Outline each blood parasite and name the species.
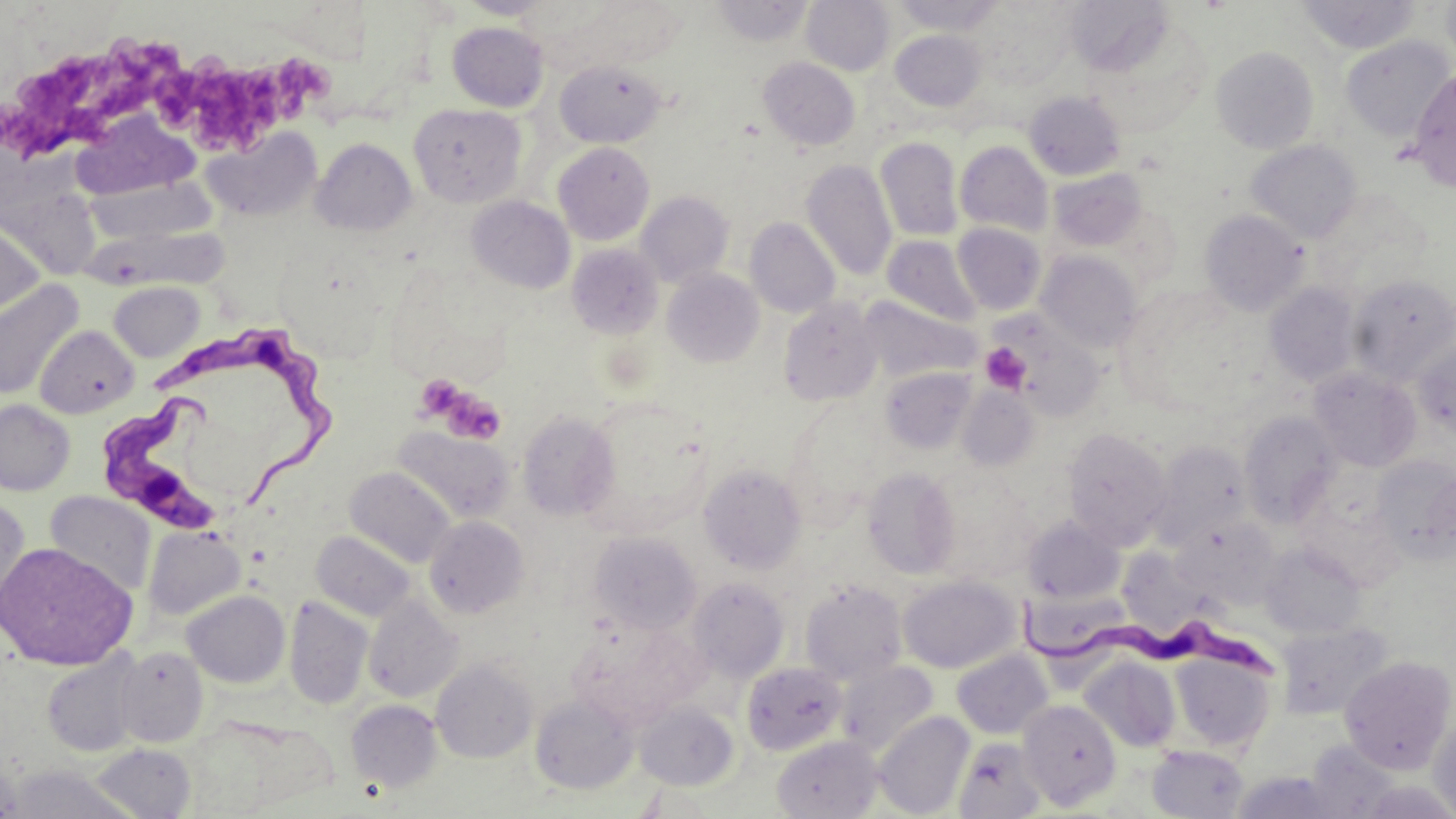

Approximate bounding boxes as named x1/y1/x2/y2 corners in pixels.
Trypanosoma brucei: (x1=154, y1=325, x2=332, y2=505), (x1=100, y1=397, x2=228, y2=534), (x1=1016, y1=596, x2=1282, y2=688).
No Plasmodium falciparum, Plasmodium ovale, Plasmodium malariae, Plasmodium vivax, or Babesia divergens observed.

Platelet locations: (x1=0, y1=34, x2=173, y2=157), (x1=154, y1=50, x2=331, y2=144), (x1=979, y1=343, x2=1031, y2=394), (x1=414, y1=374, x2=463, y2=420), (x1=438, y1=387, x2=506, y2=445). Uninfected red blood cell locations: (x1=459, y1=0, x2=552, y2=19), (x1=711, y1=0, x2=815, y2=47), (x1=801, y1=0, x2=894, y2=75), (x1=890, y1=0, x2=1006, y2=35), (x1=1296, y1=0, x2=1421, y2=54), (x1=1441, y1=0, x2=1456, y2=74), (x1=575, y1=2, x2=686, y2=67), (x1=968, y1=2, x2=1080, y2=90), (x1=1065, y1=2, x2=1195, y2=99), (x1=447, y1=22, x2=548, y2=112), (x1=890, y1=30, x2=986, y2=111), (x1=1339, y1=35, x2=1455, y2=143), (x1=1211, y1=45, x2=1319, y2=154), (x1=758, y1=57, x2=861, y2=151), (x1=555, y1=60, x2=667, y2=148), (x1=1407, y1=67, x2=1456, y2=192), (x1=1023, y1=90, x2=1126, y2=181), (x1=409, y1=104, x2=525, y2=207), (x1=70, y1=112, x2=198, y2=201), (x1=203, y1=127, x2=322, y2=221), (x1=875, y1=136, x2=964, y2=241), (x1=311, y1=138, x2=417, y2=235), (x1=1246, y1=139, x2=1363, y2=243), (x1=955, y1=141, x2=1053, y2=237), (x1=553, y1=142, x2=655, y2=245), (x1=801, y1=159, x2=896, y2=282), (x1=1049, y1=168, x2=1148, y2=251), (x1=85, y1=177, x2=215, y2=243), (x1=0, y1=181, x2=119, y2=274), (x1=635, y1=190, x2=734, y2=287), (x1=466, y1=195, x2=576, y2=294), (x1=1199, y1=209, x2=1309, y2=316), (x1=0, y1=215, x2=45, y2=319), (x1=745, y1=217, x2=840, y2=318), (x1=952, y1=222, x2=1047, y2=315), (x1=87, y1=228, x2=239, y2=289), (x1=882, y1=235, x2=982, y2=326), (x1=567, y1=244, x2=663, y2=339), (x1=1036, y1=251, x2=1144, y2=353), (x1=662, y1=269, x2=764, y2=368), (x1=1348, y1=273, x2=1455, y2=383), (x1=0, y1=279, x2=84, y2=401), (x1=109, y1=281, x2=204, y2=362), (x1=1265, y1=282, x2=1361, y2=387), (x1=858, y1=297, x2=980, y2=383), (x1=778, y1=299, x2=883, y2=406), (x1=992, y1=312, x2=1107, y2=422), (x1=36, y1=325, x2=139, y2=418), (x1=1412, y1=335, x2=1456, y2=440), (x1=879, y1=366, x2=976, y2=454), (x1=1308, y1=366, x2=1421, y2=472), (x1=957, y1=384, x2=1039, y2=471), (x1=576, y1=398, x2=713, y2=538), (x1=0, y1=399, x2=75, y2=495), (x1=781, y1=401, x2=886, y2=521), (x1=517, y1=411, x2=620, y2=521), (x1=1239, y1=411, x2=1342, y2=526), (x1=393, y1=426, x2=515, y2=524), (x1=1062, y1=426, x2=1172, y2=548), (x1=1151, y1=441, x2=1253, y2=548), (x1=1372, y1=456, x2=1456, y2=560), (x1=699, y1=463, x2=806, y2=574), (x1=345, y1=466, x2=457, y2=568), (x1=862, y1=466, x2=961, y2=579), (x1=922, y1=469, x2=1037, y2=581), (x1=45, y1=492, x2=156, y2=598), (x1=0, y1=495, x2=30, y2=618), (x1=1021, y1=515, x2=1125, y2=605), (x1=424, y1=516, x2=530, y2=618), (x1=1173, y1=517, x2=1281, y2=604), (x1=143, y1=527, x2=245, y2=620), (x1=311, y1=531, x2=416, y2=622), (x1=589, y1=531, x2=702, y2=634), (x1=1114, y1=541, x2=1216, y2=637), (x1=0, y1=542, x2=137, y2=670), (x1=1260, y1=542, x2=1366, y2=639), (x1=898, y1=574, x2=1020, y2=673), (x1=687, y1=577, x2=789, y2=682), (x1=800, y1=580, x2=907, y2=684), (x1=182, y1=590, x2=290, y2=688), (x1=363, y1=595, x2=463, y2=703), (x1=1027, y1=596, x2=1130, y2=690), (x1=283, y1=597, x2=373, y2=710), (x1=570, y1=620, x2=705, y2=729), (x1=1275, y1=621, x2=1392, y2=720), (x1=115, y1=646, x2=208, y2=747), (x1=952, y1=649, x2=1053, y2=739), (x1=41, y1=650, x2=144, y2=757), (x1=1170, y1=652, x2=1276, y2=752), (x1=1339, y1=655, x2=1455, y2=773), (x1=1080, y1=656, x2=1181, y2=752), (x1=431, y1=659, x2=537, y2=763), (x1=837, y1=660, x2=938, y2=756), (x1=741, y1=662, x2=847, y2=755), (x1=530, y1=693, x2=640, y2=794), (x1=1019, y1=699, x2=1122, y2=809), (x1=346, y1=700, x2=443, y2=793), (x1=634, y1=701, x2=739, y2=790), (x1=1428, y1=710, x2=1456, y2=816), (x1=873, y1=711, x2=974, y2=818), (x1=772, y1=735, x2=883, y2=818), (x1=953, y1=736, x2=1047, y2=819), (x1=1303, y1=740, x2=1401, y2=817), (x1=91, y1=743, x2=197, y2=818), (x1=1147, y1=745, x2=1249, y2=819), (x1=8, y1=764, x2=135, y2=819), (x1=1230, y1=770, x2=1344, y2=818). Slide-level diagnosis: Trypanosoma brucei. Optical microscopy. Image is 1456×819 pixels. Captured at 1000x magnification. May-Grünwald-Giemsa stain. Single field of view. Thin blood film.